Outline each blood parasite and name the species.
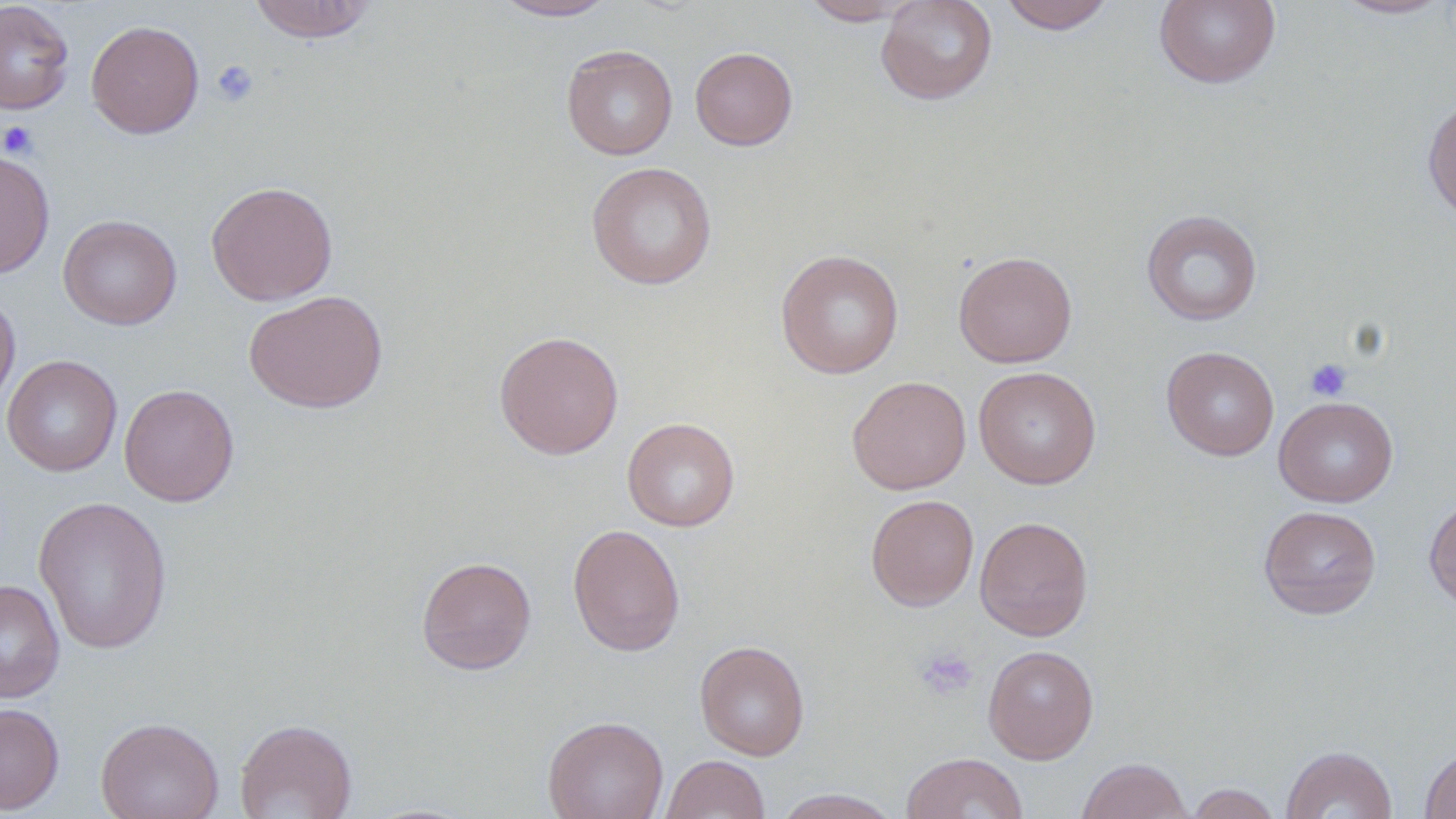

No blood parasites seen.

Approximate bounding boxes as (x1,y1)-(x2,y2) corner pairs in pixels. Uninfected red blood cell locations: (247,0)-(379,43), (800,0)-(916,25), (875,0)-(998,105), (999,0)-(1115,34), (1153,0)-(1281,88), (1330,0)-(1454,20), (0,1)-(75,115), (493,1)-(618,21), (86,20)-(204,139), (561,44)-(678,160), (690,46)-(798,150), (1422,96)-(1456,223), (0,148)-(55,279), (586,162)-(717,290), (206,181)-(338,306), (1141,209)-(1262,326), (58,214)-(183,330), (775,249)-(904,379), (953,251)-(1077,368), (0,290)-(20,419), (244,290)-(388,413), (494,330)-(624,459), (1161,346)-(1279,461), (1,355)-(123,477), (973,366)-(1102,489), (846,375)-(971,495), (118,384)-(240,507), (1273,396)-(1399,507), (622,417)-(740,531), (866,494)-(979,611), (1424,495)-(1456,615), (33,496)-(173,654), (1258,505)-(1381,620), (974,516)-(1093,641), (567,523)-(685,657), (416,556)-(537,675), (0,579)-(65,704), (694,640)-(810,761), (983,644)-(1099,764), (0,702)-(64,814), (542,715)-(669,819), (96,716)-(224,819), (235,718)-(358,819), (1281,745)-(1397,819), (1420,747)-(1456,819), (901,752)-(1029,818), (661,754)-(771,818), (1077,757)-(1192,819), (1185,783)-(1283,819), (772,788)-(902,819). Platelet locations: (210,59)-(259,107), (0,120)-(39,159), (1304,358)-(1353,402), (914,645)-(978,701). Slide-level diagnosis: negative for blood parasites. Thin blood smear. One field of a larger specimen. 1000x magnification. Light microscopy. Image is 1456×819 pixels. May-Grünwald-Giemsa-stained preparation.